Classify this cell by malaria status.
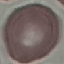
It is uninfected.

stain = Giemsa
image type = cell patch, automatically extracted from a larger field of view and resized to 64 × 64 pixels
capture = smartphone through the microscope eyepiece
preparation = thin smear